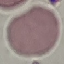

Summary:
  - Result: no malaria parasites seen
  - Stain: Giemsa
  - Capture: smartphone camera at the microscope eyepiece
  - Image type: automatically extracted cell patch, resized to 64 × 64 pixels
  - Preparation: thin blood smear